Assess the morphology of the red blood cells.
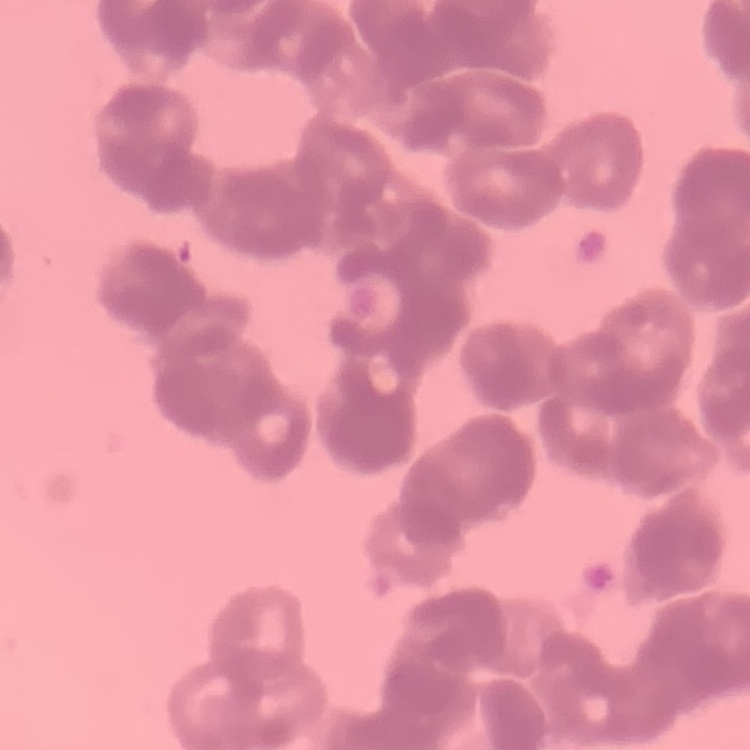

Rouleaux formation.

Summary:
  - Stain: Field's or Giemsa
  - Preparation: thin peripheral smear
  - Image type: square crop of a larger photomicrograph